Assess this cell for malaria.
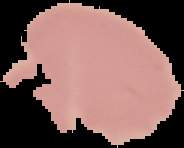
It is uninfected.

preparation: thin blood smear
image_size: 184×148 pixels
image_type: segmented cell region on a black background